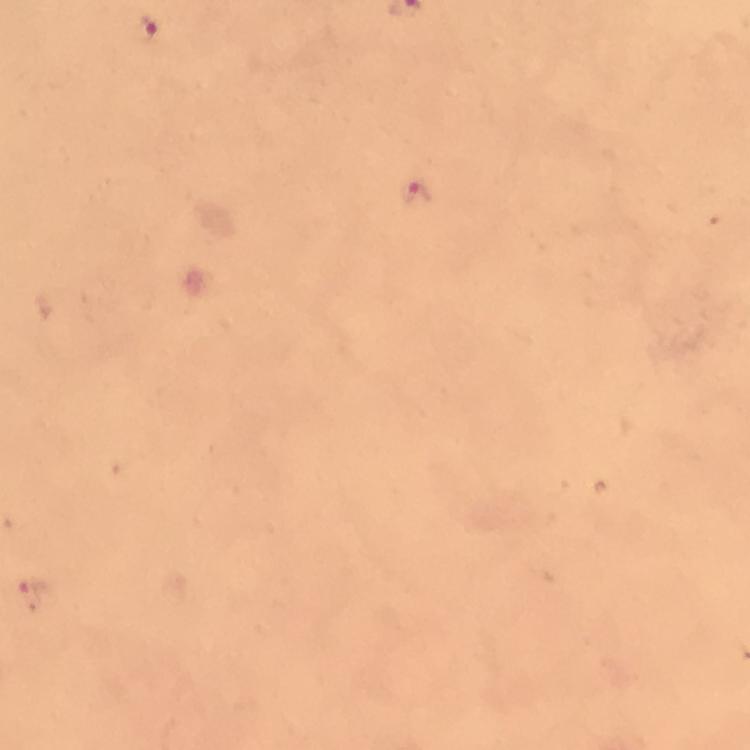
Approximate centers as (x, y) in pixels.
Summary:
  - Malaria parasite locations: (145, 31), (418, 192), (33, 595)
  - Context: from a diagnostic examination for malaria
  - Stain: Giemsa
  - Preparation: thick blood smear
  - Image size: 750×750 pixels
  - Cropped from: one field of view
  - Capture: smartphone photograph through a microscope
  - Immersion oil: applied
  - Magnification: 100x